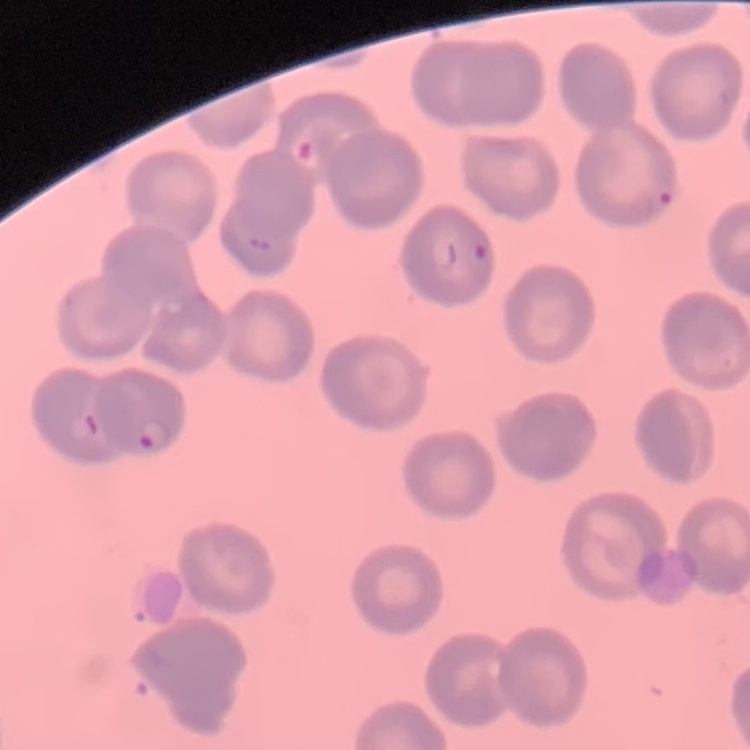
Summary:
  - Red blood cell morphology: no rouleaux formation
  - Stain: Field's or Giemsa
  - Preparation: thin blood film
  - Image type: one tile cut from a larger photomicrograph